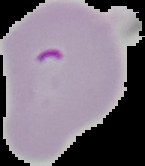

preparation = thin blood smear
result = malaria parasites detected
image type = segmented cell region on a black background
image size = 145×166 pixels